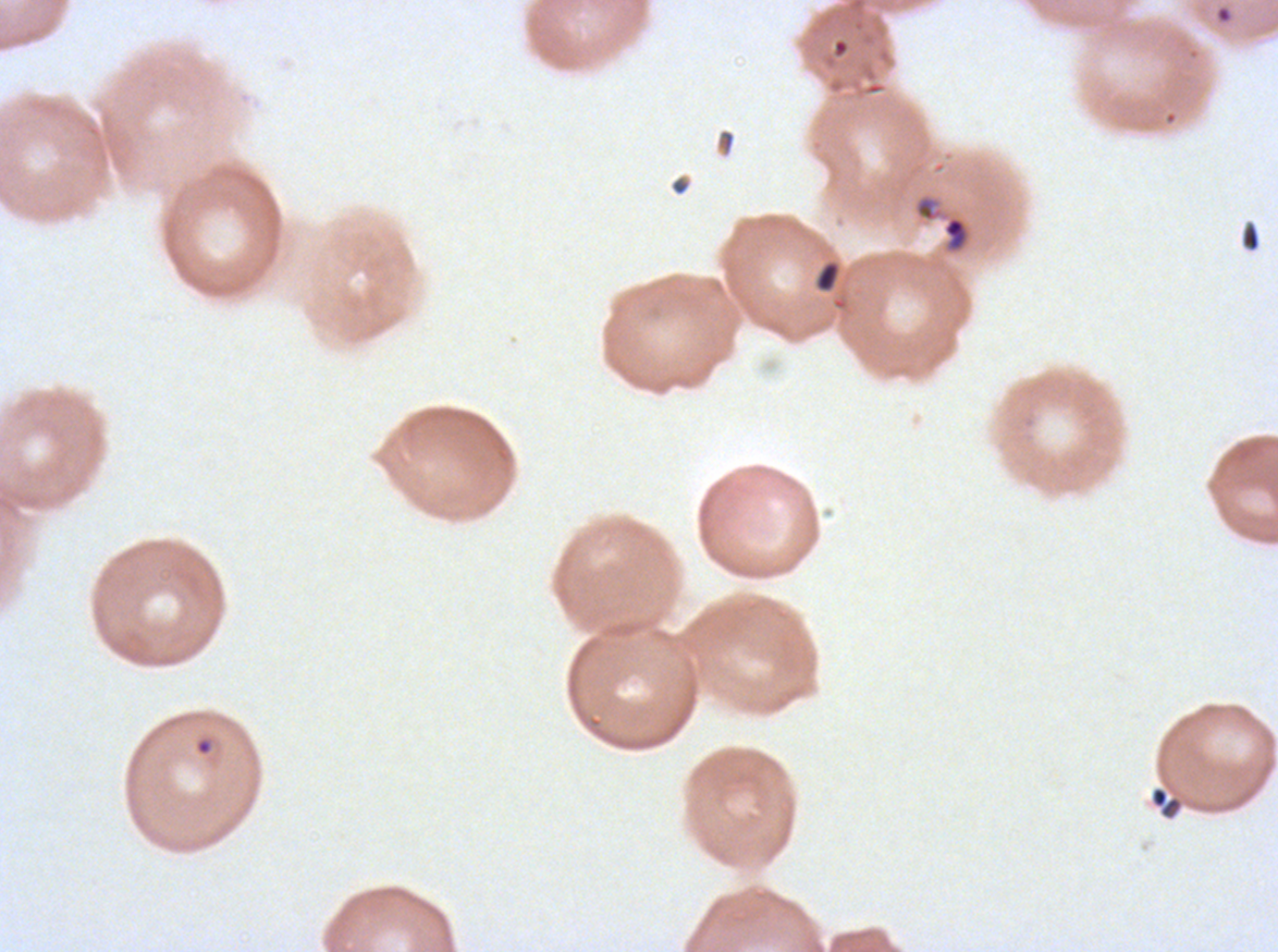

{
  "preparation": "thin blood film",
  "stain": "Giemsa",
  "image_size": "1278×952 pixels",
  "specimen": "P. falciparum from a patient in The Gambia, cultured ex vivo for 24 to 48 hours",
  "field_of_view": "sub-image separated from a larger composite",
  "ring_locations": "approximate bounding boxes as [x1, y1, x2, y2] in pixels: [1214, 5, 1234, 24], [194, 737, 214, 756]",
  "debris_locations": "approximate bounding boxes as [x1, y1, x2, y2] in pixels: [832, 38, 850, 58], [914, 193, 972, 256], [1240, 222, 1260, 252], [815, 261, 841, 293], [1149, 786, 1185, 821]"
}